Assess this cell for malaria.
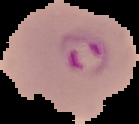
It is parasitized.

Summary:
  - Image type: segmented cell region with the area outside set to black
  - Image size: 139×124 pixels
  - Preparation: thin blood film